Assess this cell for malaria.
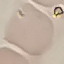

Uninfected.

Photographed with a smartphone camera at the microscope eyepiece. Automatically extracted cell patch, resized to 64 × 64 pixels. Giemsa stain. Thin blood film.